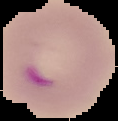
Summary:
  - Image size: 118×121 pixels
  - Preparation: thin blood film
  - Image type: cell region segmented out of the field of view; surrounding area masked to black
  - Result: malaria parasites identified